Comment on the morphology of the red blood cells.
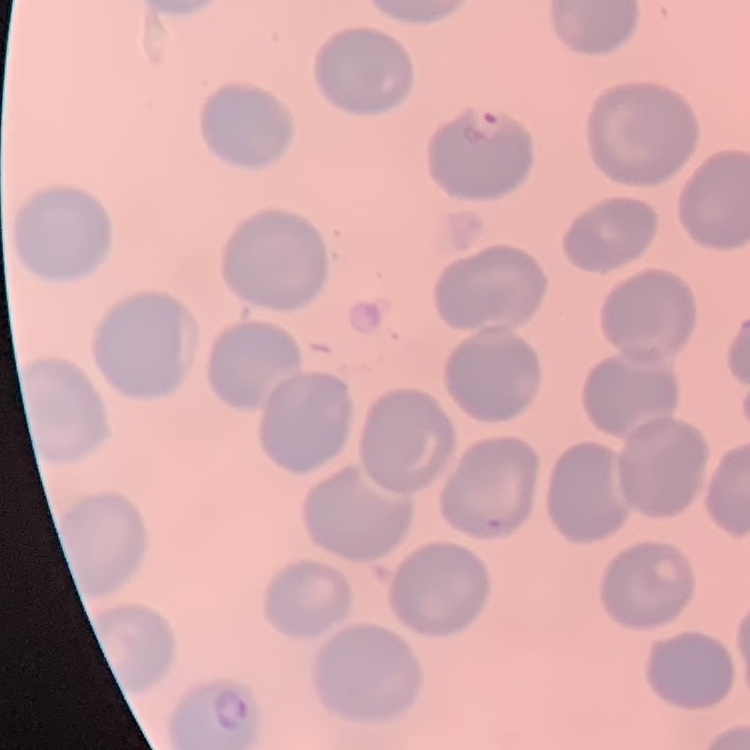

No rouleaux formation.

Field's or Giemsa stain. Square crop of a larger photomicrograph. Thin peripheral smear.